State which parasite is depicted.
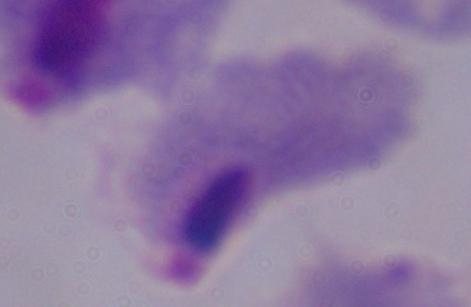

This is a trichomonad.

Captured at 1000x magnification. Photomicrograph.